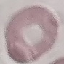
Malaria status: uninfected. Thin blood smear. Automatically extracted cell patch, resized to 64 × 64 pixels. Acquired by smartphone through the microscope eyepiece. Giemsa-stained preparation.